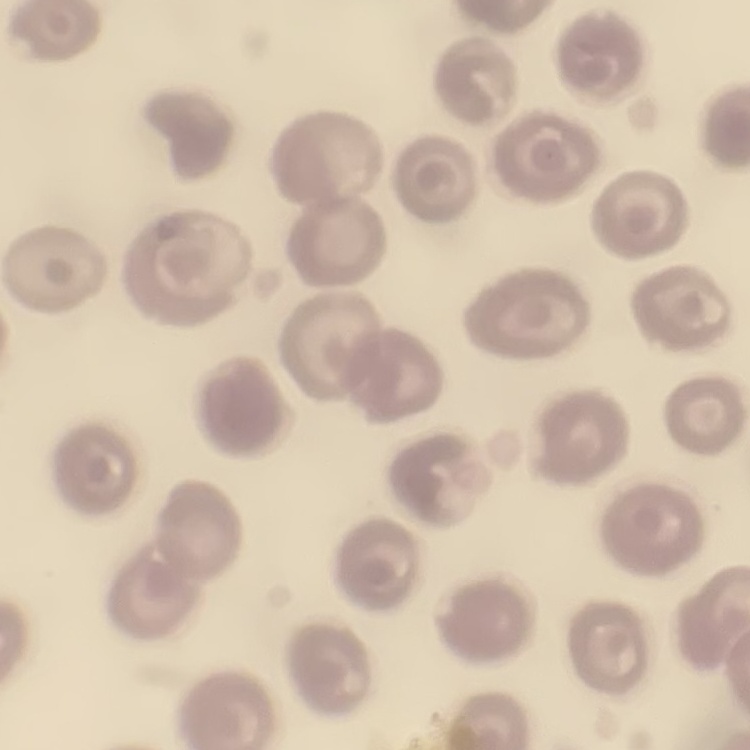
The red blood cells show no rouleaux formation. Stained with either Field's or Giemsa. One tile cut from a larger photomicrograph. Thin peripheral smear.